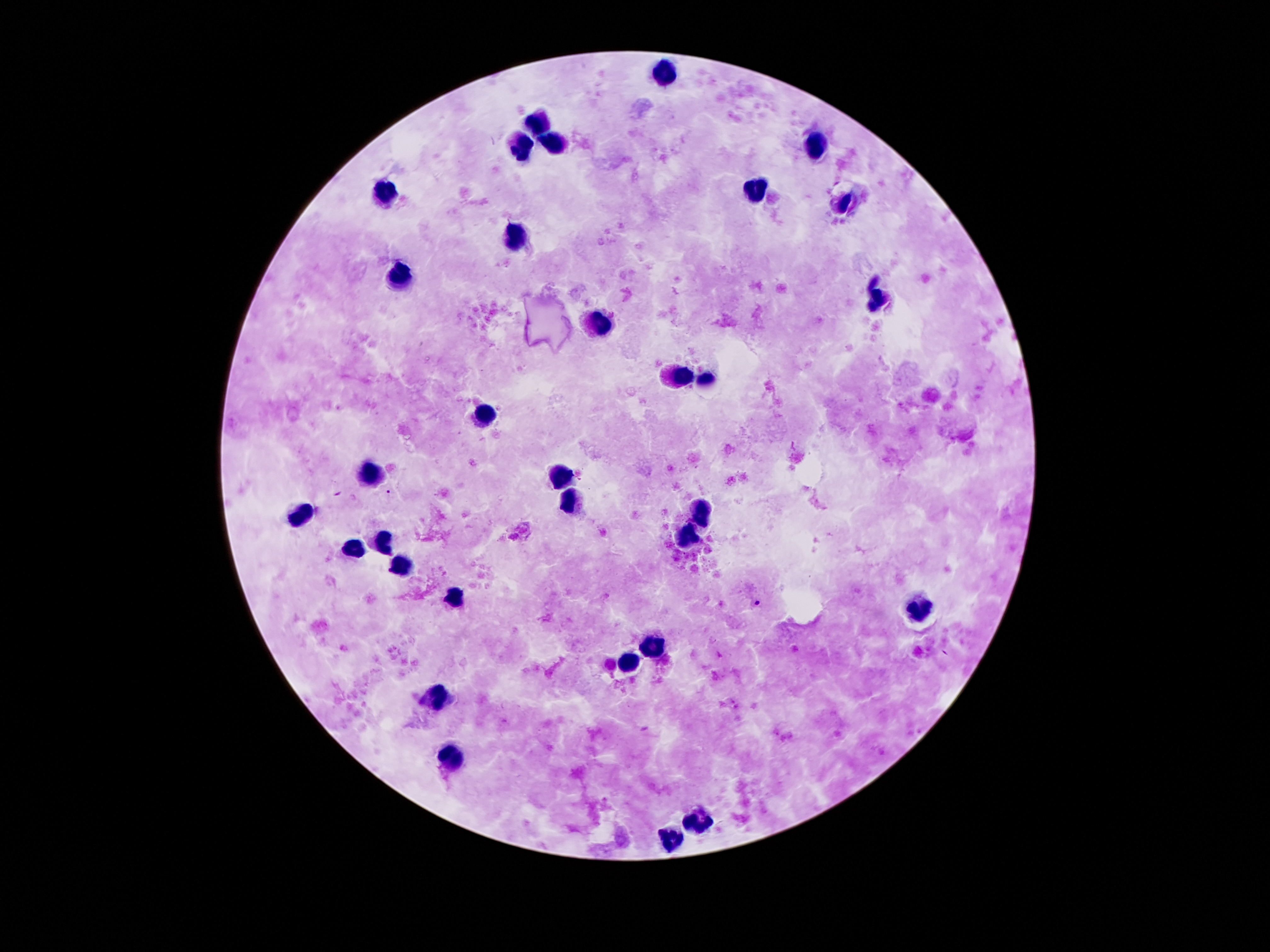
Approximate centers as [x, y] in pixels.
Summary:
  - Leukocyte locations: [663, 75], [542, 125], [556, 139], [518, 146], [817, 148], [759, 186], [388, 190], [843, 202], [513, 235], [401, 274], [876, 299], [603, 324], [678, 377], [705, 380], [487, 413], [373, 470], [558, 474], [570, 503], [306, 510], [703, 510], [686, 540], [387, 548], [349, 549], [405, 563], [456, 596], [919, 609], [652, 647], [629, 658], [433, 698], [459, 755], [698, 815], [672, 834]
  - Preparation: thick peripheral-blood smear
  - Field of view: single
  - Capture: smartphone camera through the microscope eyepiece
  - Patient malaria status: not infected
  - Magnification: 100x
  - Image size: 1270×952 pixels
  - Stain: Giemsa